Classify this cell by malaria status.
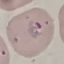

It is parasitized.

Summary:
  - Image type: automatically extracted cell patch, resized to 64 × 64 pixels
  - Preparation: thin blood smear
  - Stain: Giemsa
  - Capture: smartphone through the microscope eyepiece